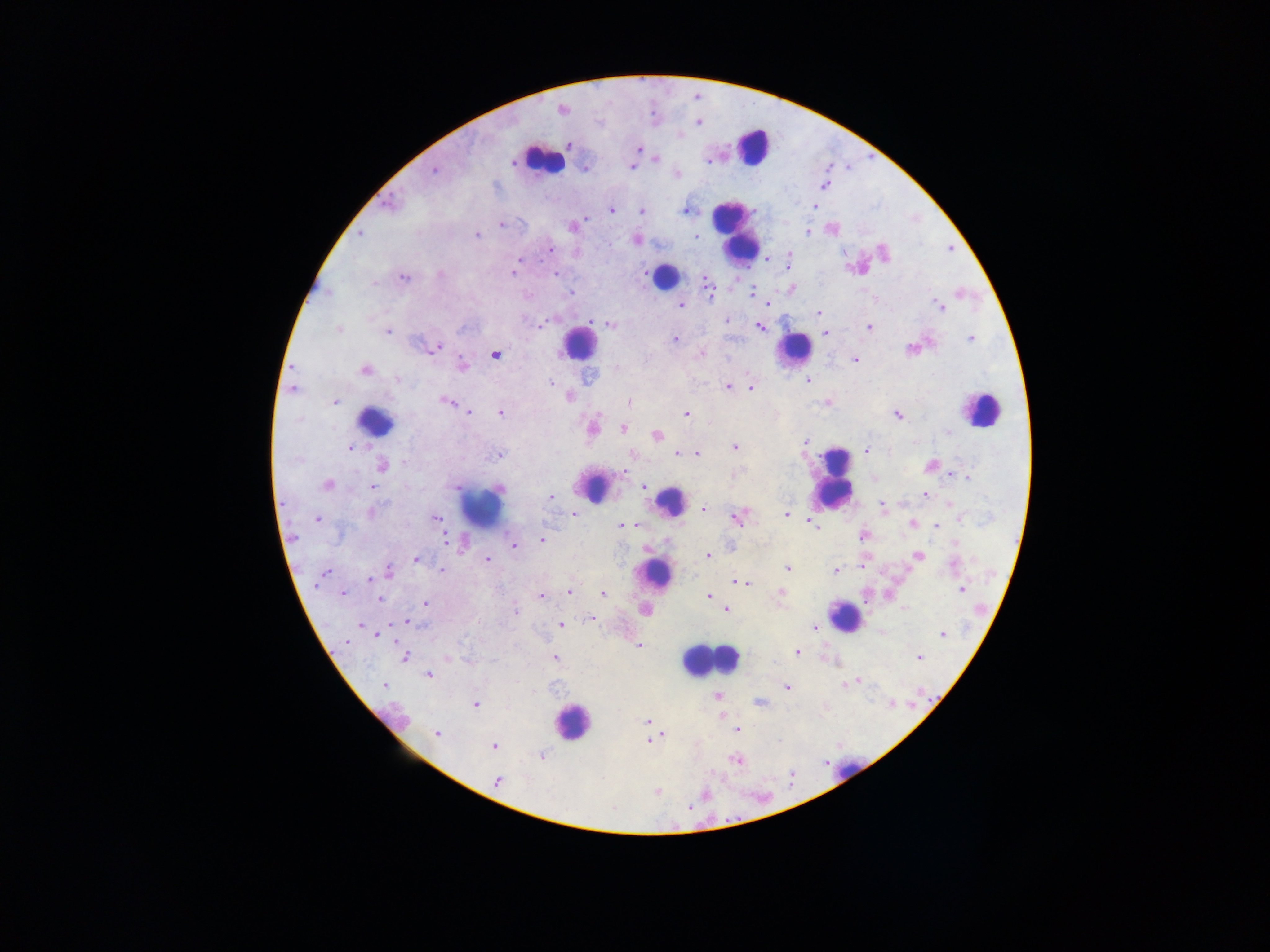
Approximate centers as (x, y) in pixels.
Summary:
  - Plasmodium parasite locations: (561, 109), (698, 122), (568, 144), (638, 149), (655, 158), (709, 161), (631, 167), (585, 168), (434, 170), (823, 186), (389, 203), (813, 206), (611, 209), (687, 210), (641, 211), (500, 224), (573, 226), (695, 232), (807, 232), (360, 234), (476, 234), (697, 236), (636, 240), (549, 249), (789, 255), (764, 260), (788, 263), (513, 273), (555, 273), (403, 277), (791, 289), (708, 291), (570, 293), (750, 294), (768, 303), (680, 305), (940, 307), (819, 313), (725, 321), (610, 323), (539, 325), (759, 327), (868, 327), (337, 328), (387, 331), (824, 332), (676, 338), (971, 339), (913, 346), (434, 348), (495, 353), (700, 353), (854, 359), (460, 365), (365, 369), (807, 380), (550, 382), (727, 386), (750, 387), (292, 389), (568, 397), (445, 401), (334, 402), (630, 402), (828, 402), (468, 412), (500, 412), (687, 414), (897, 414), (591, 428), (623, 428), (656, 435), (804, 441), (735, 446), (349, 448), (866, 450), (677, 453), (684, 453), (696, 453), (497, 454), (633, 454), (382, 465), (930, 465), (623, 472), (952, 473), (966, 476), (873, 478), (327, 485), (456, 485), (371, 487), (644, 487), (925, 494), (551, 497), (949, 502), (882, 507), (702, 510), (371, 512), (572, 514), (787, 514), (738, 517), (318, 518), (434, 518), (810, 523), (636, 524), (912, 524), (814, 525), (621, 526), (935, 526), (863, 535), (445, 539), (542, 540), (955, 542), (514, 545), (707, 555), (918, 555), (416, 559), (487, 559), (861, 565), (787, 568), (441, 570), (836, 570), (326, 572), (388, 572), (382, 575), (370, 579), (738, 581), (746, 582), (750, 583), (962, 588), (569, 591), (780, 592), (343, 593), (603, 594), (541, 596), (709, 596), (379, 598), (425, 603), (645, 609), (727, 609), (515, 611), (591, 618), (407, 621), (361, 624), (560, 624), (814, 628), (376, 634), (942, 634), (344, 641), (638, 645), (797, 653), (919, 656), (405, 657), (555, 657), (428, 674), (859, 679), (385, 685), (846, 685), (787, 687), (716, 696), (759, 702), (475, 704), (646, 722), (737, 729), (437, 733), (663, 735), (647, 739), (493, 746), (542, 755), (738, 759), (497, 780), (656, 791)
  - Leukocyte locations: (752, 147), (542, 159), (734, 230), (663, 276), (578, 343), (794, 348), (981, 410), (375, 421), (832, 480), (593, 486), (671, 501), (480, 506), (654, 574), (845, 615), (709, 660), (571, 723), (849, 769)
  - Image size: 1270×952 pixels
  - Preparation: thick blood smear
  - Country: Ghana
  - Field of view: single
  - Capture: mobile-phone photograph through a microscope